Name the parasite shown.
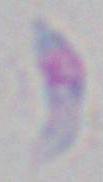

Toxoplasma gondii.

Summary:
  - Modality: photomicrograph
  - Magnification: 1000x